Comment on the morphology of the erythrocytes.
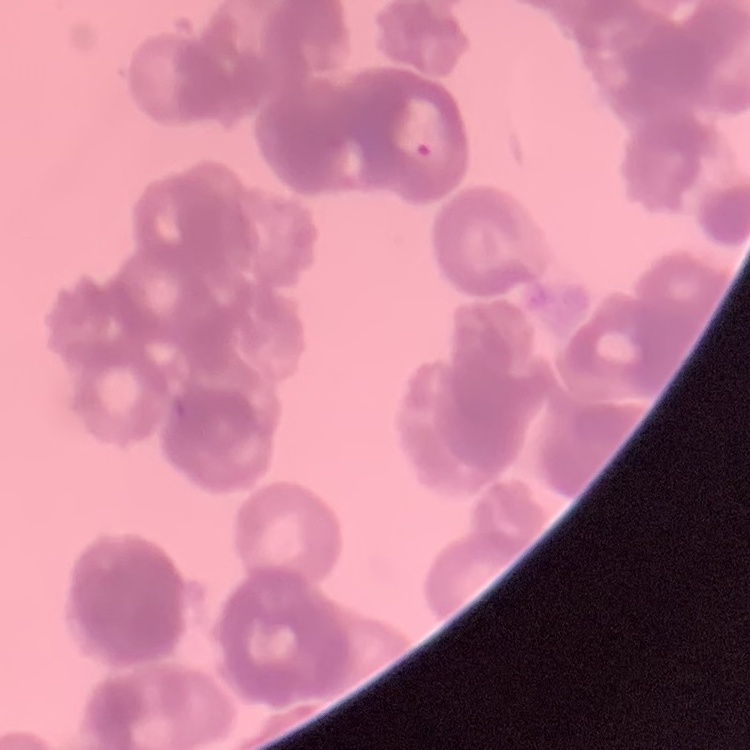
They show rouleaux formation.

{
  "image_type": "one tile cut from a larger photomicrograph",
  "stain": "Field's or Giemsa",
  "preparation": "thin blood film"
}